Identify the blood parasite species.
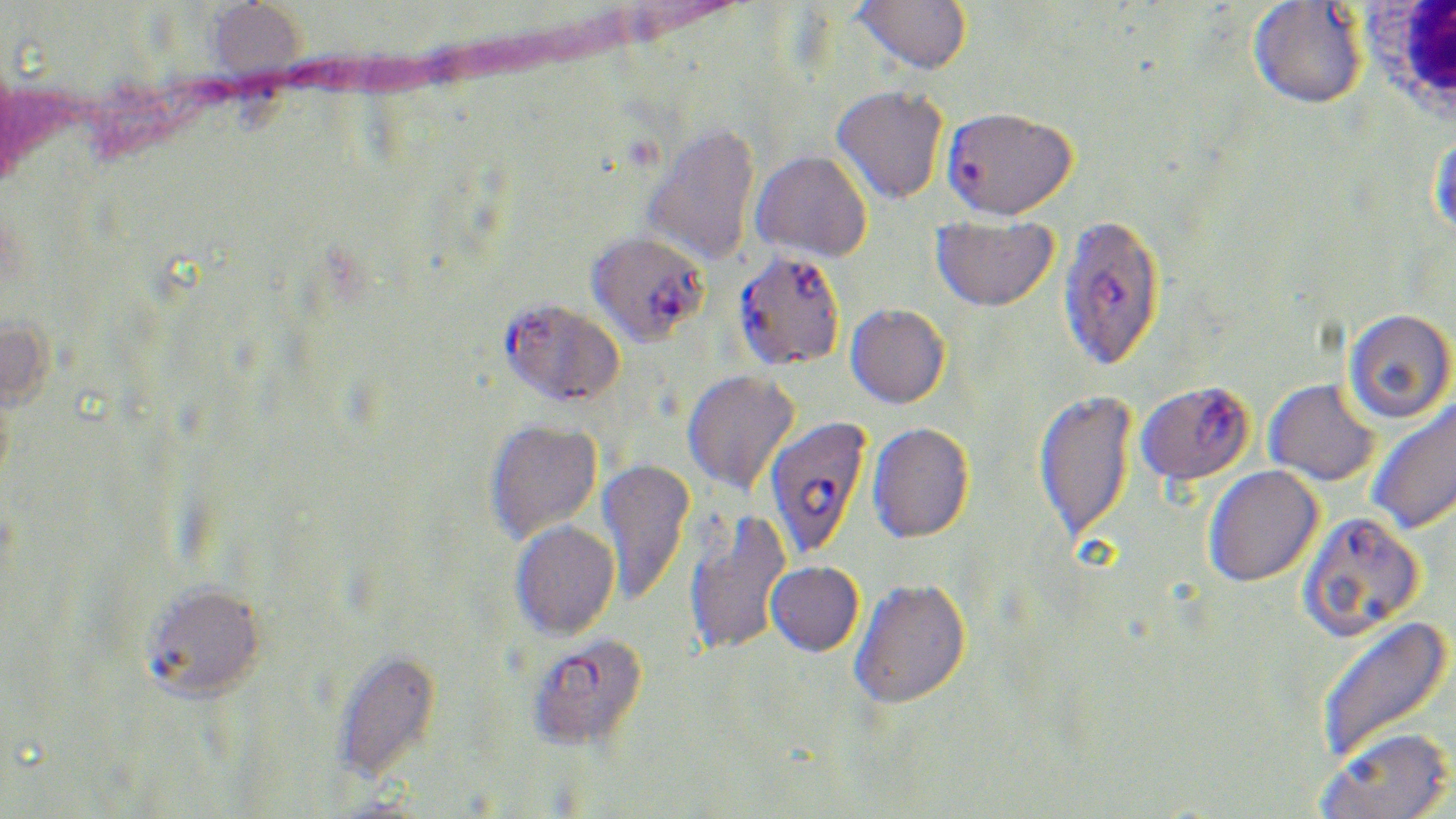

Plasmodium falciparum.

Approximate bounding boxes as [x1, y1, x2, y2] in pixels. Plasmodium falciparum-infected red blood cell locations: [941, 106, 1077, 221], [1058, 212, 1165, 371], [586, 229, 709, 345], [733, 249, 846, 371], [499, 298, 625, 407], [1136, 380, 1255, 485], [764, 416, 872, 560], [1297, 510, 1424, 641], [528, 632, 650, 751]. Uninfected red blood cell locations: [851, 0, 972, 75], [204, 1, 307, 86], [1249, 1, 1367, 109], [831, 84, 949, 205], [642, 123, 760, 267], [1429, 133, 1456, 242], [751, 150, 872, 263], [931, 215, 1059, 311], [846, 303, 950, 408], [1343, 308, 1455, 424], [682, 369, 799, 494], [1264, 379, 1380, 486], [1034, 388, 1137, 547], [1366, 397, 1456, 536], [484, 418, 603, 543], [867, 421, 974, 544], [596, 457, 695, 604], [1203, 465, 1323, 587], [682, 507, 791, 658], [510, 519, 619, 641], [766, 561, 864, 656], [849, 577, 971, 709], [141, 580, 267, 702], [1314, 614, 1453, 765], [332, 648, 442, 783], [1317, 725, 1454, 819]. White blood cell locations: [1362, 0, 1456, 121]. May-Grünwald-Giemsa-stained preparation. Light microscopy. Image is 1456×819 pixels. One field of a larger specimen. Captured at 1000x magnification. Thin blood smear.